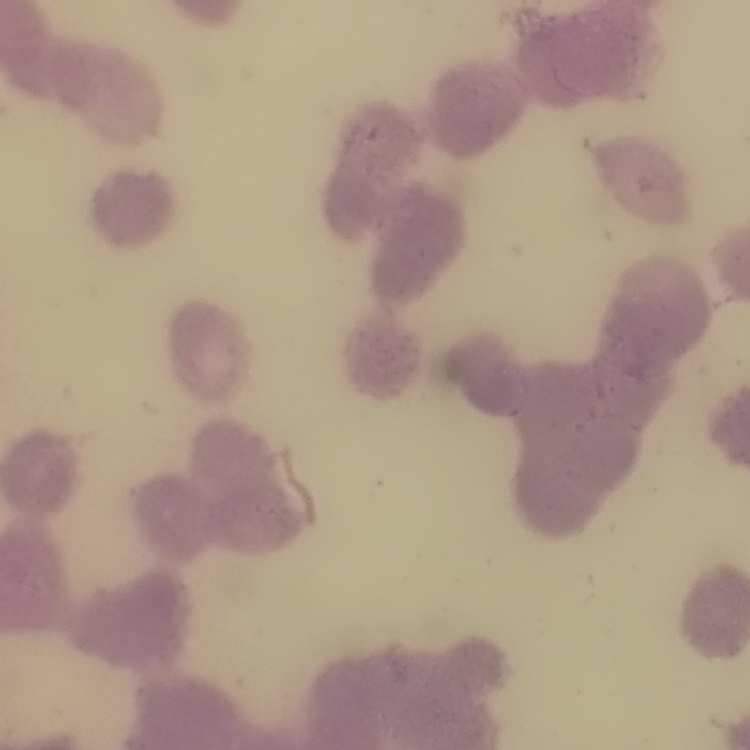 The red blood cells show rouleaux formation. One tile cut from a larger photomicrograph. Stained with either Field's or Giemsa. Thin blood film.